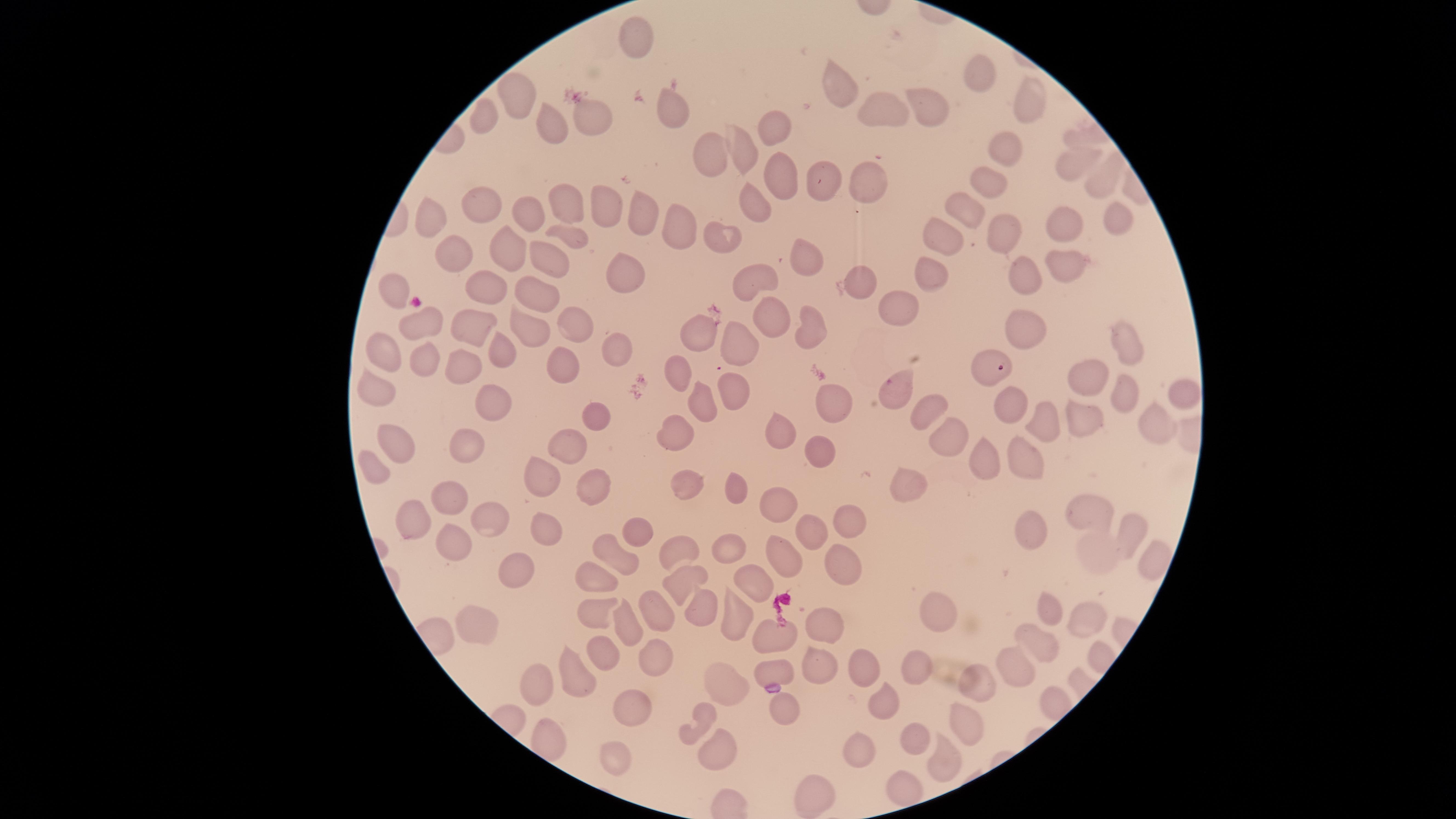 Approximate marker points as [x, y] in pixels. Parasitized red blood cells: [993, 368]. Uninfected red blood cells: [631, 42], [982, 76], [842, 89], [1022, 101], [520, 102], [929, 107], [670, 114], [886, 115], [596, 120], [489, 124], [555, 125], [773, 128], [1083, 135], [740, 149], [1002, 149], [711, 156], [1068, 167], [779, 176], [867, 178], [827, 182], [986, 184], [1097, 184], [754, 201], [481, 207], [567, 208], [604, 208], [967, 213], [526, 214], [641, 215], [1119, 218], [439, 222], [676, 228], [1067, 228], [724, 233], [1002, 233], [572, 234], [941, 235], [503, 246], [555, 252], [804, 260], [456, 261], [1061, 263], [621, 270], [1019, 277], [931, 278], [758, 283], [863, 284], [491, 286], [392, 290], [547, 294], [901, 313], [479, 324], [775, 324], [808, 326], [528, 328], [1024, 328], [421, 333], [581, 333], [705, 333], [1119, 338], [738, 350], [384, 351], [503, 351], [618, 351], [564, 365], [420, 366], [458, 371], [1094, 374], [679, 377], [1123, 384], [373, 385], [902, 393], [734, 394], [1184, 394], [493, 400], [835, 402], [709, 404], [924, 408], [1016, 412], [1151, 419], [1087, 420], [1047, 425], [598, 428], [671, 431], [773, 433], [470, 444], [388, 449], [822, 449], [570, 450], [1024, 457], [986, 463], [372, 470], [546, 474], [682, 479], [592, 486], [901, 488], [744, 494], [452, 503], [780, 513], [1092, 517], [489, 519], [416, 522], [850, 523], [1027, 531], [637, 533], [1120, 535], [543, 538], [808, 539], [454, 545], [732, 547], [680, 550], [1094, 553], [838, 556], [774, 557], [618, 567], [1151, 567], [522, 571], [679, 579], [754, 582], [595, 589], [1046, 606], [651, 613], [700, 613], [490, 616], [940, 616], [1085, 616], [736, 618], [597, 621], [817, 621], [632, 631], [773, 642], [1037, 643], [598, 655], [647, 659], [864, 664], [1018, 665], [916, 670], [810, 673], [781, 674], [577, 682], [738, 687], [973, 687], [541, 693], [891, 705], [634, 708], [782, 713], [708, 719], [961, 729], [916, 741], [714, 752], [865, 754], [939, 758], [614, 760], [808, 785], [908, 793]. Giemsa-stained preparation. Presence: malaria parasites seen. One field of view of the specimen. Thin smear of blood. Circular visible region. Species: Plasmodium falciparum. Image is 1456×819 pixels. Smartphone photograph through the microscope eyepiece.